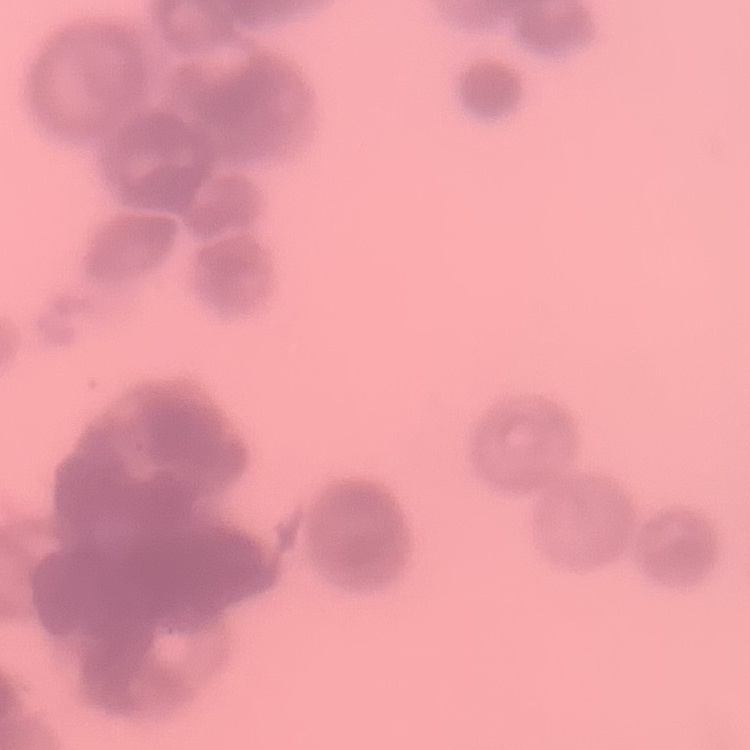

erythrocyte morphology = rouleaux formation
preparation = thin blood smear
stain = Field's or Giemsa
image type = one tile cut from a larger photomicrograph